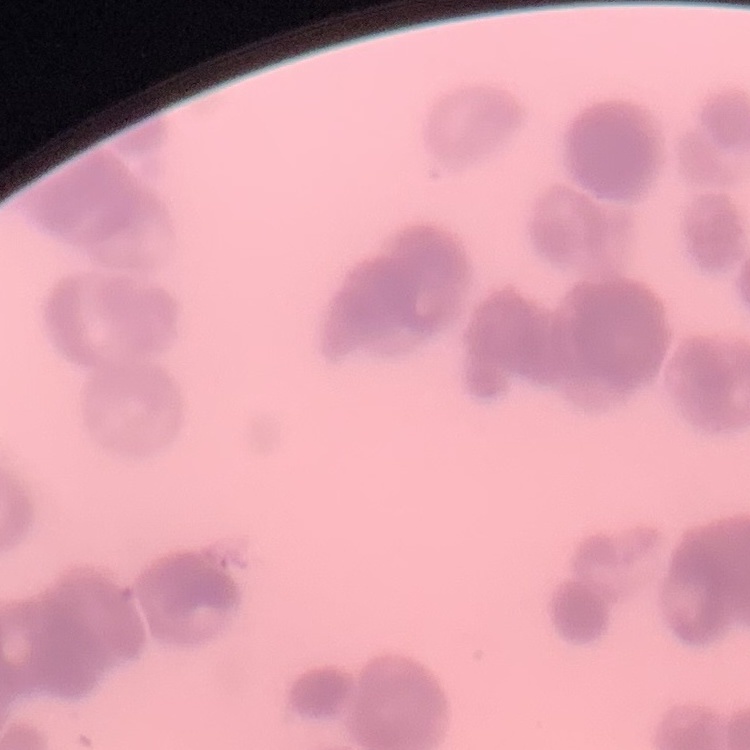
red blood cell morphology = rouleaux formation
image type = square crop of a larger photomicrograph
preparation = thin blood film
stain = Field's or Giemsa